Give the extent of all uninfected red blood cells.
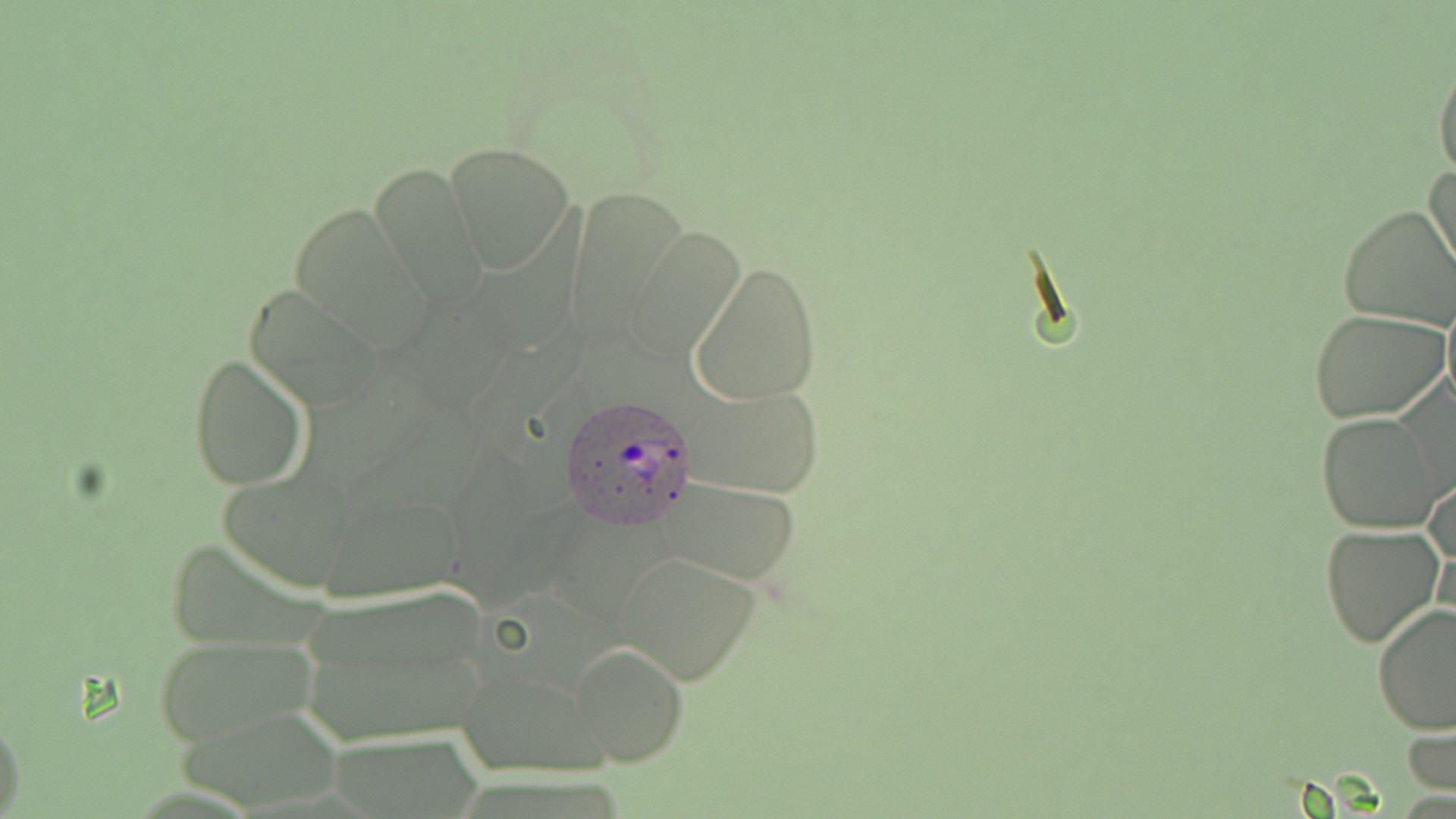

Approximate bounding boxes as (x1, y1, x2, y2) in pixels.
Uninfected red blood cells: (1433, 52, 1456, 181), (444, 142, 576, 274), (365, 161, 488, 309), (1427, 167, 1456, 286), (287, 200, 437, 351), (1337, 203, 1456, 331), (625, 228, 747, 361), (690, 260, 823, 405), (244, 284, 386, 414), (1440, 288, 1456, 420), (1309, 309, 1450, 423), (187, 353, 310, 491), (686, 382, 826, 498), (1317, 413, 1445, 533), (1424, 467, 1455, 590), (218, 469, 362, 592), (652, 475, 808, 586), (320, 490, 464, 604), (1320, 523, 1446, 649), (613, 550, 764, 686), (295, 587, 495, 746), (1372, 603, 1456, 736), (152, 633, 317, 748), (571, 644, 687, 768), (461, 666, 607, 778), (175, 704, 349, 810), (0, 713, 24, 816), (1404, 714, 1454, 800).

Summary:
  - Plasmodium ovale-infected red blood cell locations: (557, 396, 700, 529)
  - Slide-level diagnosis: Plasmodium ovale
  - Magnification: 1000x
  - Modality: light microscopy
  - Stain: May-Grünwald-Giemsa
  - Image size: 1456×819 pixels
  - Preparation: thin blood film
  - Field of view: single